Report the malaria status of this cell.
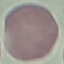
Uninfected.

Cell patch, automatically extracted from a larger field of view and resized to 64 × 64 pixels. Thin blood smear. Giemsa stain. Photographed with a smartphone camera at the microscope eyepiece.